Outline each blood parasite and name the species.
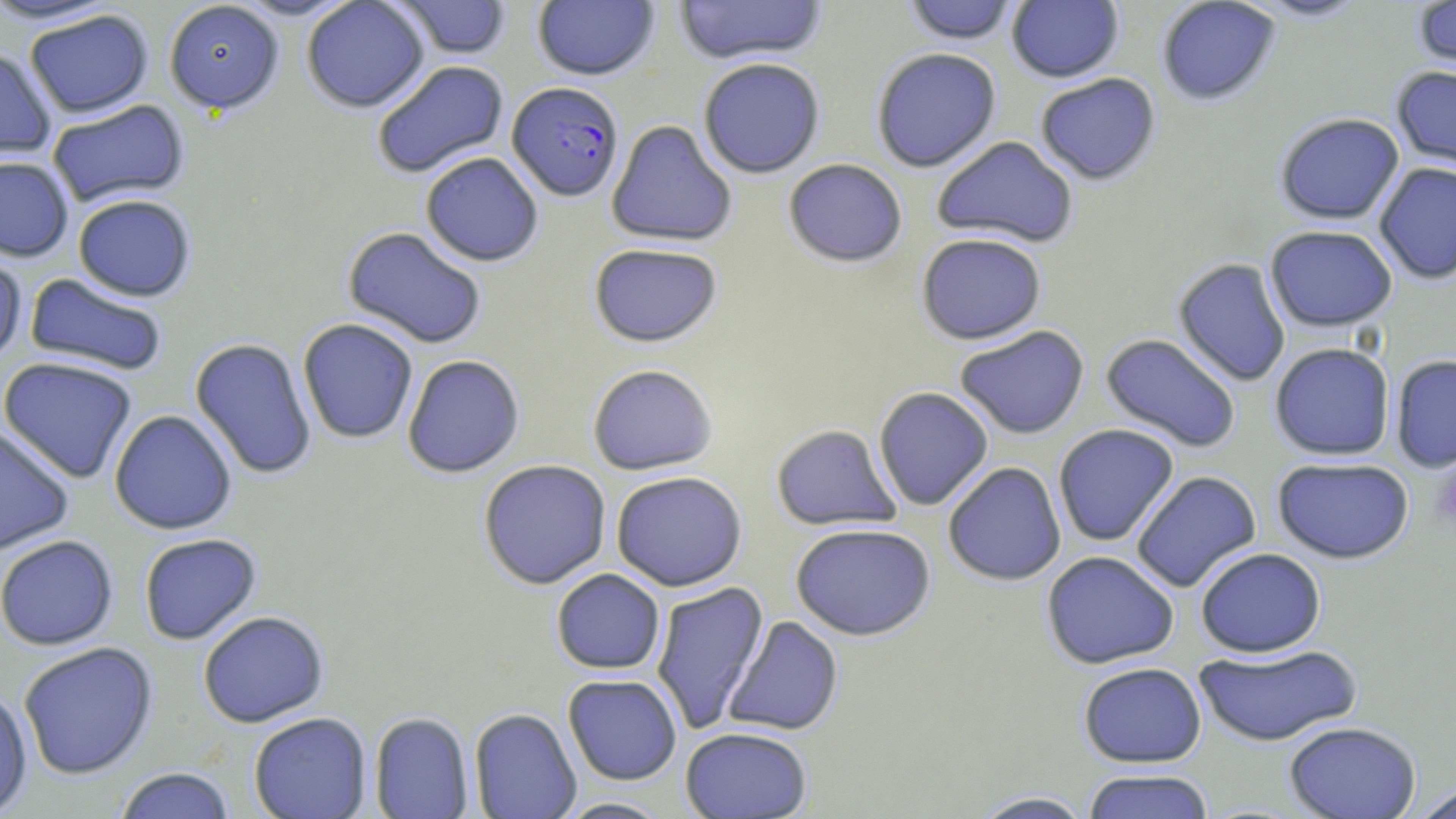
Approximate bounding boxes as (x1,y1)-(x2,y2) corner pairs in pixels.
Plasmodium falciparum-infected red blood cells: (506,81)-(625,202).
No Plasmodium ovale, Plasmodium malariae, Plasmodium vivax, Babesia divergens, or Trypanosoma brucei observed.

slide-level diagnosis = Plasmodium falciparum
magnification = 1000x
stain = May-Grünwald-Giemsa
field of view = one of a larger specimen
image size = 1456×819 pixels
modality = optical microscopy
uninfected red blood cell locations = approximate bounding boxes as (x1,y1)-(x2,y2) corner pairs in pixels: (229,0)-(362,21), (301,0)-(430,113), (532,0)-(660,82), (673,0)-(828,65), (901,0)-(1021,45), (1156,0)-(1281,107), (1245,0)-(1373,22), (1412,0)-(1456,82), (0,1)-(118,27), (163,1)-(284,116), (390,1)-(513,60), (1006,1)-(1124,83), (24,10)-(154,119), (0,46)-(56,161), (871,47)-(1001,172), (698,57)-(825,179), (371,60)-(509,180), (1391,64)-(1456,179), (1035,73)-(1161,186), (47,99)-(190,208), (1274,112)-(1405,225), (606,119)-(738,248), (931,136)-(1079,249), (420,152)-(544,267), (0,156)-(74,261), (783,158)-(908,268), (1374,161)-(1456,285), (73,194)-(197,302), (1265,225)-(1398,332), (343,226)-(487,349), (916,233)-(1047,345), (588,243)-(722,348), (0,247)-(28,369), (1173,258)-(1291,387), (24,273)-(168,376), (297,318)-(418,444), (954,325)-(1090,439), (1100,333)-(1241,454), (189,337)-(317,479), (1269,342)-(1395,461), (402,354)-(525,478), (1390,354)-(1456,473), (0,357)-(138,483), (586,364)-(718,476), (873,386)-(994,510), (109,409)-(237,535), (1053,423)-(1179,547), (770,424)-(901,531), (0,425)-(75,555), (1272,457)-(1415,564), (477,459)-(612,590), (943,461)-(1066,586), (1130,470)-(1262,593), (610,471)-(748,591), (789,523)-(937,641), (138,533)-(262,645), (0,535)-(119,651), (1195,547)-(1326,657), (1041,551)-(1179,670), (551,569)-(665,674), (651,580)-(769,736), (198,611)-(329,728), (723,615)-(843,736), (18,642)-(159,780), (1193,643)-(1363,747), (1078,662)-(1207,768), (563,674)-(682,785), (0,685)-(33,818), (469,708)-(582,819), (369,711)-(474,819), (249,712)-(372,819), (1283,721)-(1422,818), (680,727)-(812,818), (112,767)-(237,819), (1082,769)-(1216,819), (1411,783)-(1456,819), (969,790)-(1097,818), (553,797)-(675,818)
preparation = thin blood smear
platelet locations = approximate bounding boxes as (x1,y1)-(x2,y2) corner pairs in pixels: (1430,460)-(1456,532)